Give a bounding box for every parasitised red blood cell.
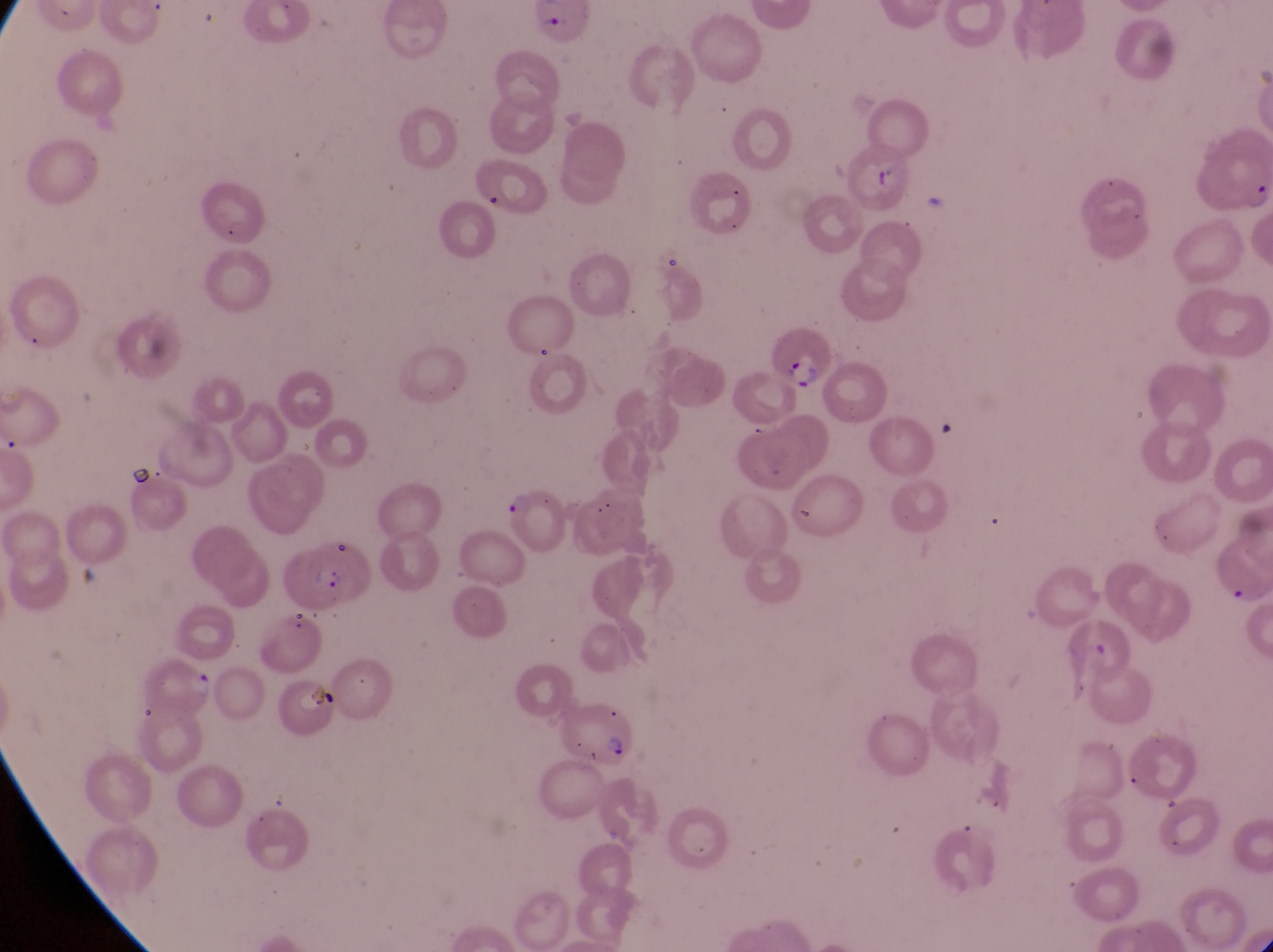
Approximate bounding boxes as {left, top, right, bottom} in pixels.
Parasitised red blood cells: {474, 155, 534, 218}, {762, 322, 827, 394}, {497, 487, 574, 569}, {275, 539, 375, 617}, {556, 704, 637, 769}.

Trophozoite locations: {180, 669, 220, 714}. Artifact (platelet-like body, stain precipitate, or debris) locations: {869, 157, 909, 200}, {307, 682, 339, 710}. Thin blood film. Single field of view. Magnification of 1000x. Captured by a smartphone held over the eyepiece of an Olympus CX-23 microscope. Collected in Uganda. Image is 1273×952 pixels.